Identify the preparation type.
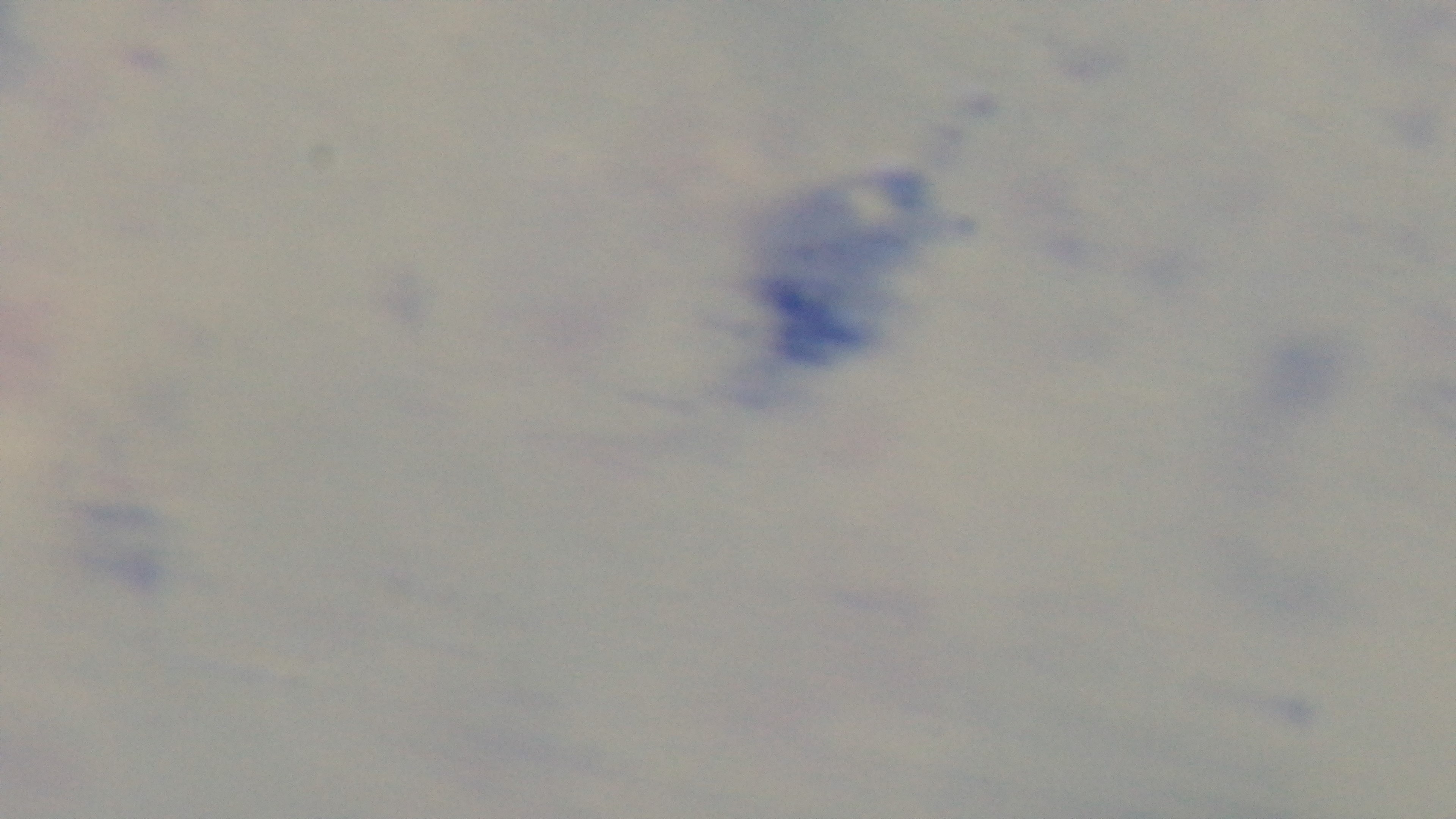
Thick.

field_of_view: one from the slide
stain: Giemsa
objective: 100x oil immersion
malaria_status: uninfected
modality: light microscopy
capture: mounted 4K digital camera